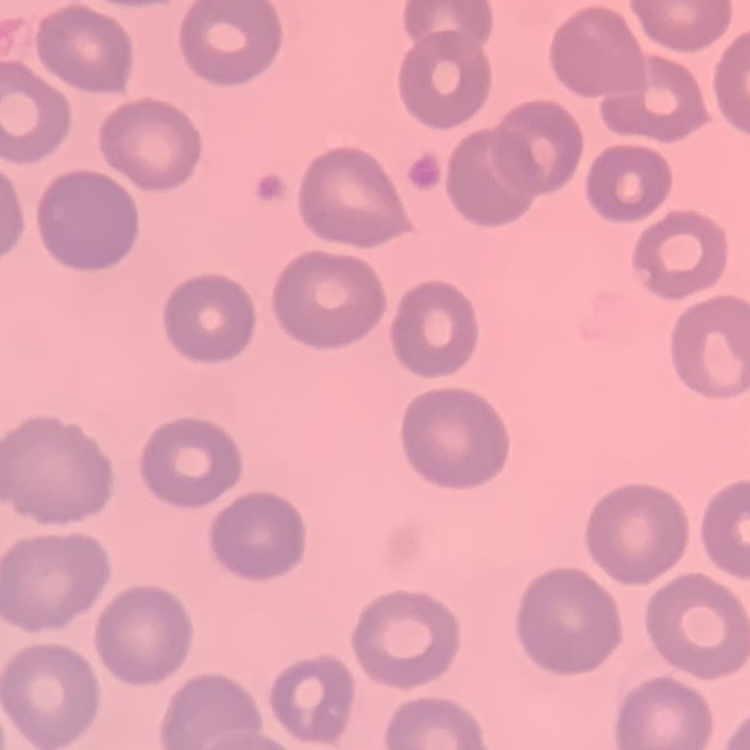

Summary:
  - Erythrocyte morphology: no rouleaux formation
  - Stain: Field's or Giemsa
  - Preparation: thin blood film
  - Image type: one tile cut from a larger photomicrograph